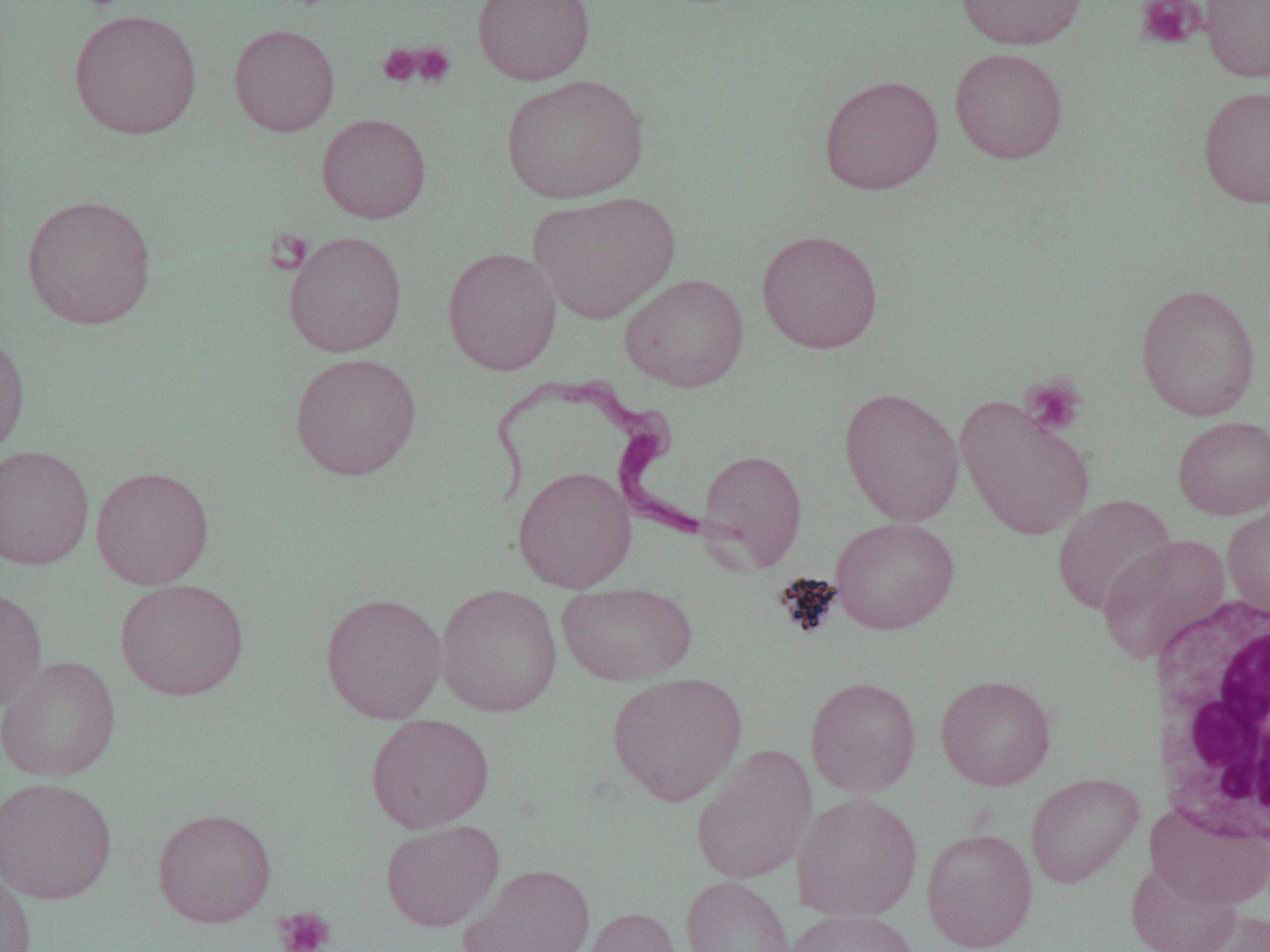

Summary:
  - Coordinate format: approximate bounding boxes as named x1/y1/x2/y2 corners in pixels
  - Platelet locations: (x1=1135, y1=0, x2=1205, y2=50), (x1=410, y1=43, x2=456, y2=88), (x1=377, y1=44, x2=421, y2=87), (x1=265, y1=229, x2=314, y2=274), (x1=1020, y1=375, x2=1088, y2=439), (x1=273, y1=907, x2=335, y2=952)
  - Uninfected red blood cell locations: (x1=473, y1=0, x2=595, y2=85), (x1=955, y1=0, x2=1088, y2=49), (x1=1200, y1=0, x2=1270, y2=82), (x1=68, y1=9, x2=202, y2=139), (x1=229, y1=23, x2=340, y2=136), (x1=949, y1=47, x2=1069, y2=164), (x1=501, y1=73, x2=649, y2=204), (x1=819, y1=74, x2=944, y2=194), (x1=1198, y1=85, x2=1270, y2=208), (x1=316, y1=113, x2=431, y2=223), (x1=528, y1=191, x2=680, y2=324), (x1=22, y1=194, x2=157, y2=330), (x1=756, y1=229, x2=883, y2=354), (x1=284, y1=231, x2=407, y2=357), (x1=442, y1=247, x2=562, y2=375), (x1=619, y1=273, x2=749, y2=392), (x1=1136, y1=283, x2=1261, y2=421), (x1=0, y1=330, x2=31, y2=458), (x1=289, y1=352, x2=421, y2=480), (x1=839, y1=386, x2=965, y2=526), (x1=955, y1=396, x2=1096, y2=540), (x1=1173, y1=415, x2=1270, y2=519), (x1=0, y1=445, x2=94, y2=570), (x1=697, y1=449, x2=808, y2=572), (x1=513, y1=465, x2=637, y2=593), (x1=91, y1=466, x2=214, y2=589), (x1=1052, y1=494, x2=1178, y2=616), (x1=1222, y1=499, x2=1270, y2=620), (x1=829, y1=516, x2=959, y2=634), (x1=1097, y1=534, x2=1231, y2=663), (x1=115, y1=578, x2=249, y2=700), (x1=557, y1=582, x2=698, y2=685), (x1=434, y1=584, x2=563, y2=717), (x1=0, y1=587, x2=47, y2=712), (x1=320, y1=592, x2=447, y2=723), (x1=0, y1=655, x2=121, y2=781), (x1=606, y1=672, x2=748, y2=806), (x1=936, y1=674, x2=1057, y2=790), (x1=805, y1=676, x2=922, y2=797), (x1=366, y1=714, x2=495, y2=833), (x1=691, y1=744, x2=818, y2=884), (x1=1025, y1=772, x2=1144, y2=888), (x1=0, y1=776, x2=117, y2=904), (x1=793, y1=792, x2=923, y2=921), (x1=1146, y1=805, x2=1270, y2=909), (x1=153, y1=807, x2=276, y2=927), (x1=380, y1=819, x2=504, y2=932), (x1=921, y1=828, x2=1038, y2=952), (x1=1125, y1=861, x2=1241, y2=952), (x1=459, y1=863, x2=596, y2=952), (x1=0, y1=866, x2=36, y2=952), (x1=681, y1=875, x2=795, y2=952), (x1=581, y1=906, x2=682, y2=952), (x1=785, y1=908, x2=920, y2=952), (x1=1189, y1=909, x2=1270, y2=952)
  - Trypanosoma brucei locations: (x1=487, y1=375, x2=708, y2=540)
  - White blood cell locations: (x1=1149, y1=594, x2=1270, y2=848)
  - Slide-level diagnosis: Trypanosoma brucei
  - Preparation: thin blood film
  - Modality: optical microscopy
  - Image size: 1270×952 pixels
  - Field of view: single
  - Magnification: 1000x